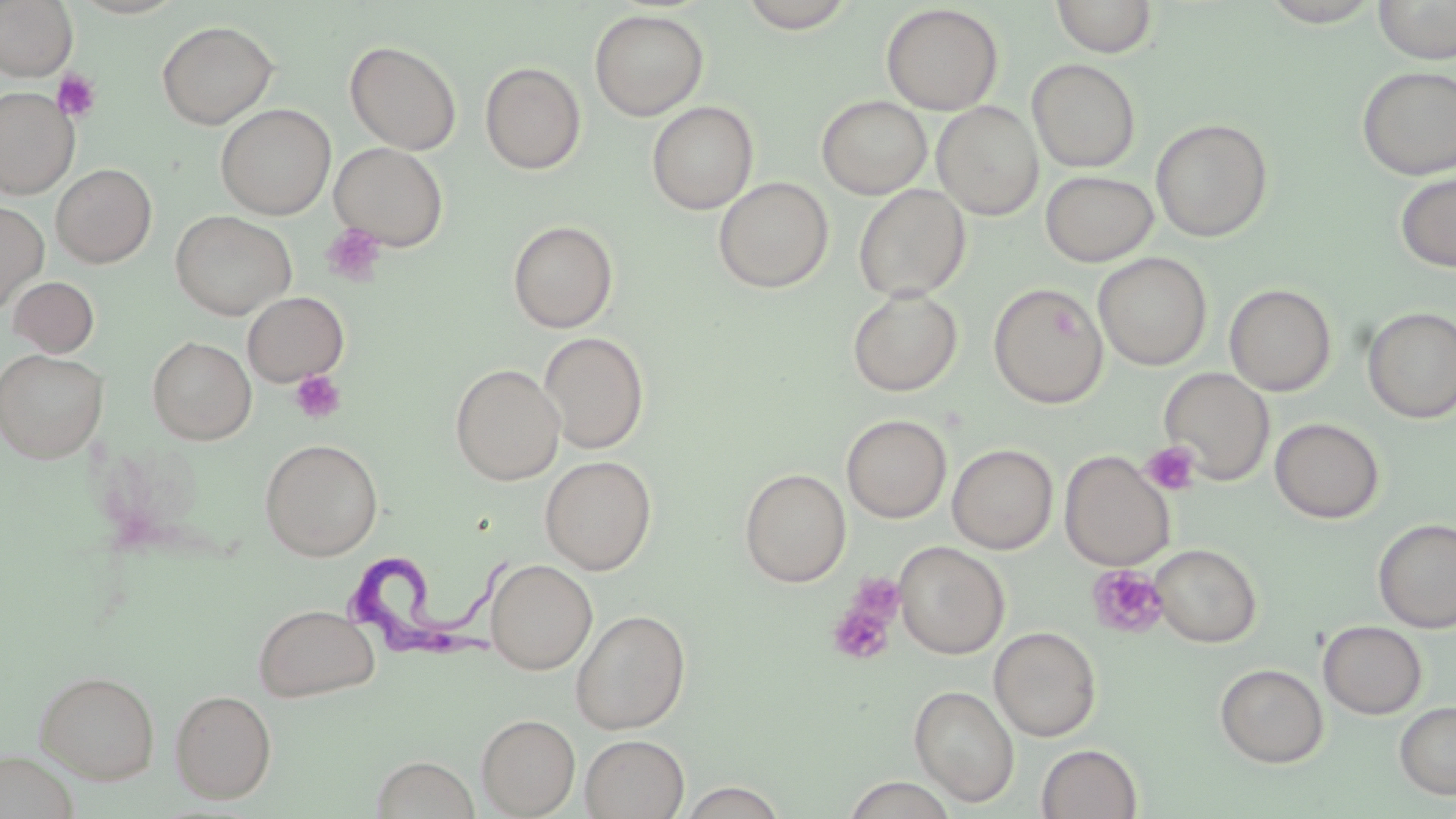
Approximate bounding boxes as (x1, y1, x2, y2) in pixels. Trypanosoma brucei locations: (335, 542, 527, 666). Uninfected red blood cell locations: (0, 0, 77, 81), (68, 0, 189, 19), (737, 0, 858, 33), (1051, 0, 1158, 58), (1259, 0, 1384, 27), (1374, 0, 1456, 64), (881, 4, 1003, 115), (589, 8, 709, 121), (157, 20, 278, 129), (344, 40, 462, 155), (1027, 59, 1141, 173), (480, 62, 586, 175), (1356, 65, 1456, 180), (0, 87, 78, 199), (816, 95, 932, 199), (647, 101, 759, 214), (932, 101, 1044, 220), (215, 104, 336, 220), (1151, 118, 1273, 242), (329, 142, 449, 251), (51, 163, 156, 267), (1040, 170, 1158, 267), (1396, 170, 1456, 272), (713, 176, 833, 294), (853, 184, 971, 301), (0, 200, 49, 314), (170, 211, 297, 321), (507, 220, 618, 333), (1094, 252, 1212, 371), (7, 276, 99, 357), (988, 283, 1108, 408), (1224, 284, 1337, 396), (847, 287, 963, 397), (242, 291, 349, 387), (1362, 307, 1456, 423), (538, 331, 650, 454), (148, 336, 256, 444), (0, 348, 107, 462), (450, 363, 565, 485), (1159, 367, 1274, 486), (841, 415, 952, 523), (1269, 418, 1384, 523), (260, 438, 382, 560), (947, 443, 1058, 554), (1059, 451, 1175, 571), (539, 454, 657, 575), (739, 468, 851, 587), (1373, 518, 1456, 634), (894, 541, 1009, 659), (1151, 543, 1261, 647), (485, 559, 597, 675), (253, 603, 380, 702), (571, 608, 690, 735), (1318, 620, 1427, 719), (989, 626, 1101, 742), (1215, 663, 1328, 767), (35, 669, 160, 784), (909, 684, 1020, 806), (170, 689, 276, 803), (1395, 700, 1456, 800), (476, 714, 580, 818), (580, 734, 689, 819), (1037, 744, 1142, 819), (0, 751, 79, 819), (370, 755, 480, 818), (677, 782, 788, 818). Platelet locations: (52, 70, 102, 122), (321, 224, 388, 286), (289, 370, 346, 423), (1140, 442, 1201, 496), (1086, 564, 1169, 639), (826, 587, 901, 667). Slide-level diagnosis: Trypanosoma brucei. Single field of view. Thin blood smear. Optical microscopy. May-Grünwald-Giemsa stain. 1000x magnification. Image is 1456×819 pixels.